Assess this cell for malaria.
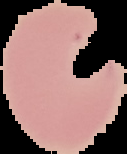

It is parasitized.

Cell region segmented out of the field of view; the surrounding area is masked to black. Image is 127×154 pixels. From a thin blood film.